Point out every malaria parasite.
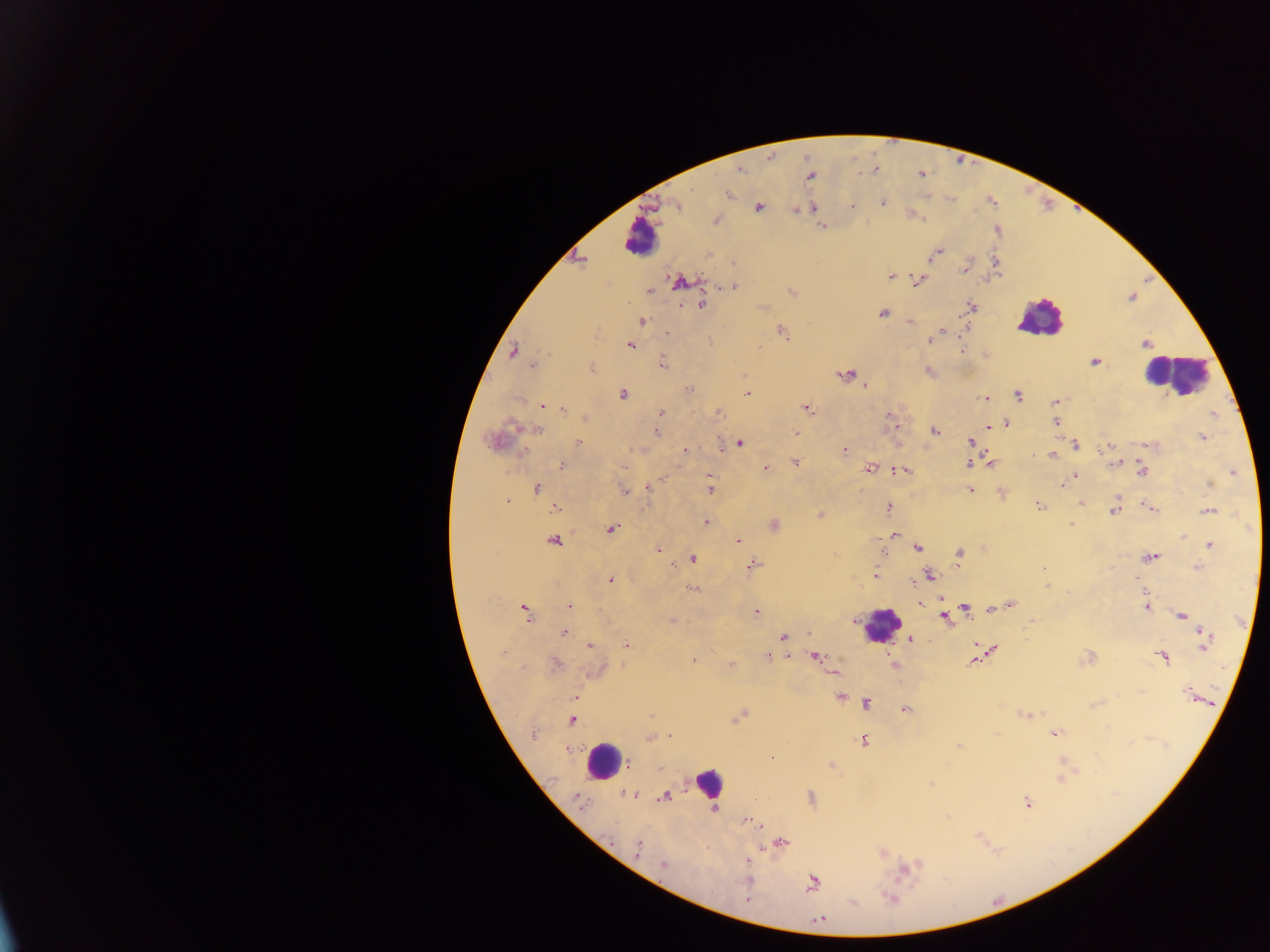
Approximate centers as (x, y) in pixels.
Malaria parasites: (739, 169), (875, 170), (810, 177), (728, 194), (883, 202), (676, 205), (851, 207), (759, 208), (813, 208), (716, 220), (821, 228), (939, 252), (931, 256), (580, 260), (996, 263), (964, 269), (891, 276), (917, 280), (681, 281), (732, 286), (649, 291), (792, 293), (703, 304), (971, 307), (883, 313), (642, 321), (910, 322), (967, 327), (781, 330), (941, 330), (665, 333), (940, 334), (929, 341), (1146, 344), (630, 345), (961, 350), (512, 351), (1094, 362), (662, 363), (532, 366), (928, 371), (845, 374), (865, 386), (690, 389), (623, 394), (748, 394), (1018, 396), (985, 398), (1056, 402), (541, 405), (563, 409), (807, 409), (661, 412), (717, 412), (1214, 413), (585, 417), (1056, 422), (1007, 423), (894, 426), (987, 426), (537, 430), (935, 431), (656, 432), (796, 433), (1203, 437), (492, 441), (971, 441), (578, 442), (740, 443), (1076, 445), (719, 446), (1106, 448), (844, 450), (685, 451), (522, 452), (1052, 456), (989, 462), (795, 463), (969, 463), (1114, 463), (562, 466), (765, 468), (869, 469), (904, 470), (1141, 471), (1233, 473), (1075, 475), (1210, 484), (1062, 485), (536, 487), (648, 488), (709, 489), (970, 490), (624, 491), (508, 501), (1082, 503), (1039, 506), (555, 507), (889, 508), (1149, 508), (1114, 510), (1208, 511), (820, 514), (707, 522), (1071, 524), (774, 525), (611, 529), (894, 535), (738, 539), (554, 540), (1210, 545), (918, 548), (658, 549), (959, 554), (1150, 557), (693, 559), (959, 561), (672, 565), (753, 565), (1199, 567), (1043, 568), (930, 575), (875, 577), (1137, 579), (610, 580), (694, 588), (941, 600), (919, 604), (1010, 605), (569, 606), (1147, 607), (965, 608), (994, 608), (523, 609), (756, 613), (526, 614), (1182, 615), (944, 617), (672, 620), (1031, 623), (564, 634), (808, 634), (783, 637), (910, 639), (1204, 640), (626, 644), (590, 645), (992, 650), (502, 653), (816, 656), (768, 657), (1163, 657), (1087, 658), (693, 659), (972, 661), (894, 664), (556, 665), (731, 665), (594, 672), (1141, 691), (1186, 693), (839, 697), (573, 698), (867, 704), (905, 709), (1025, 714), (651, 716), (740, 716), (571, 721), (1056, 733), (533, 734), (670, 736), (649, 738), (864, 741), (959, 747), (830, 765), (1061, 777), (931, 785), (627, 794), (665, 796), (580, 798), (1027, 802), (746, 821), (754, 823), (783, 843), (637, 847), (663, 865), (907, 868), (747, 880), (812, 883), (890, 898), (747, 900), (820, 920).

Summary:
  - Leukocyte locations: (640, 236), (1040, 318), (1174, 373), (881, 625), (605, 760), (709, 782)
  - Capture: mobile-phone photograph through a microscope
  - Preparation: thick blood smear
  - Image size: 1270×952 pixels
  - Country: Ghana
  - Field of view: single